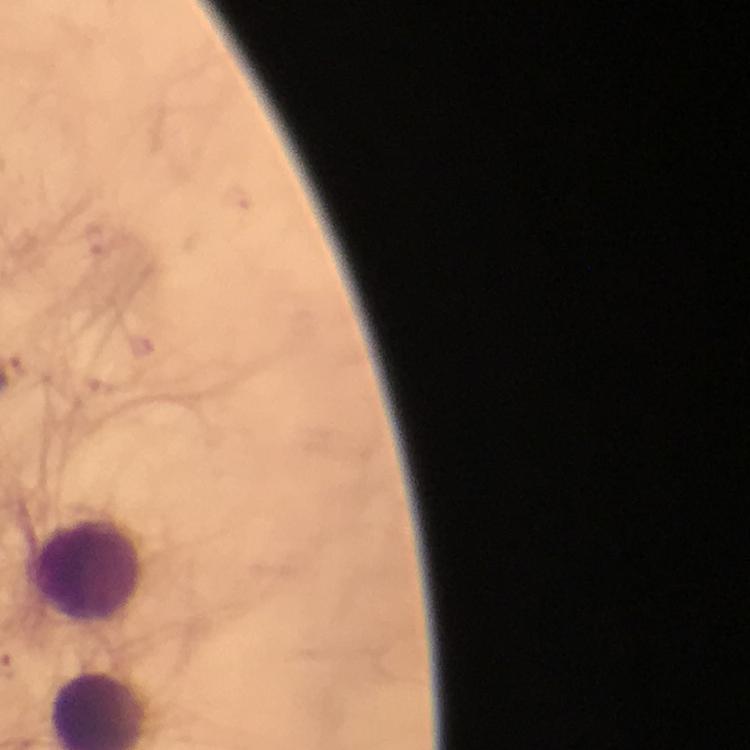
Approximate centers as [x, y] in pixels.
Summary:
  - Leukocyte locations: [89, 568]
  - Malaria parasite locations: [94, 240], [139, 344], [29, 370]
  - Immersion oil: used
  - Cropped from: one field of view
  - Context: from a malaria diagnostic workup
  - Preparation: thick blood smear
  - Stain: Giemsa
  - Magnification: 100x
  - Capture: smartphone mounted on the microscope
  - Image size: 750×750 pixels